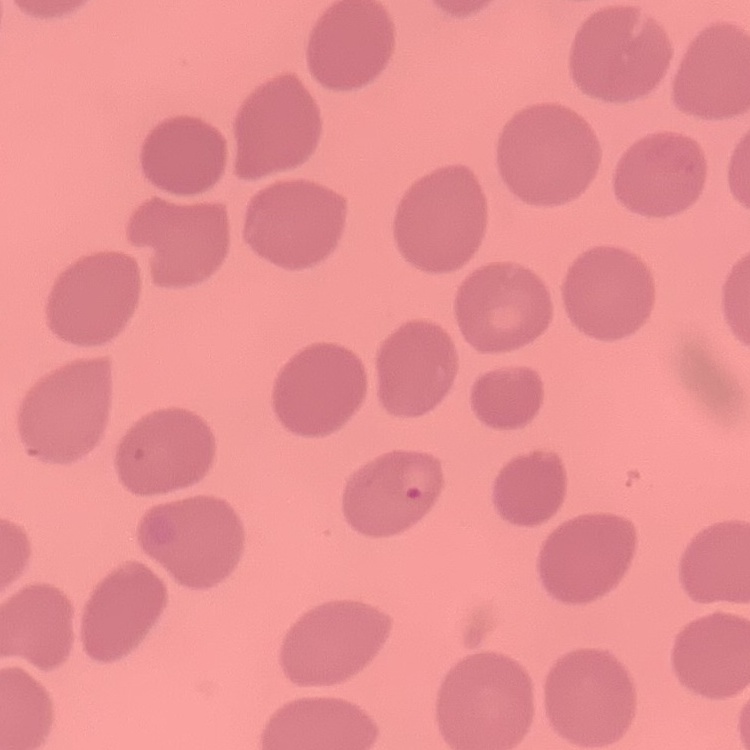
Summary:
  - Red blood cell morphology: no rouleaux formation
  - Image type: one tile cut from a larger photomicrograph
  - Stain: Field's or Giemsa
  - Preparation: thin blood smear